Comment on the morphology of the red blood cells.
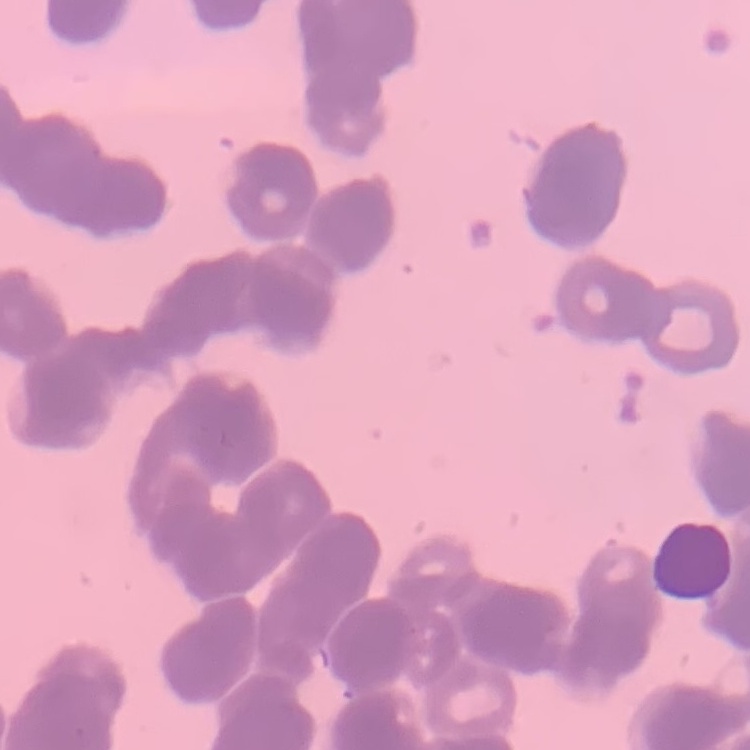
They show rouleaux formation.

image_type: one tile cut from a larger photomicrograph
preparation: thin peripheral smear
stain: Field's or Giemsa